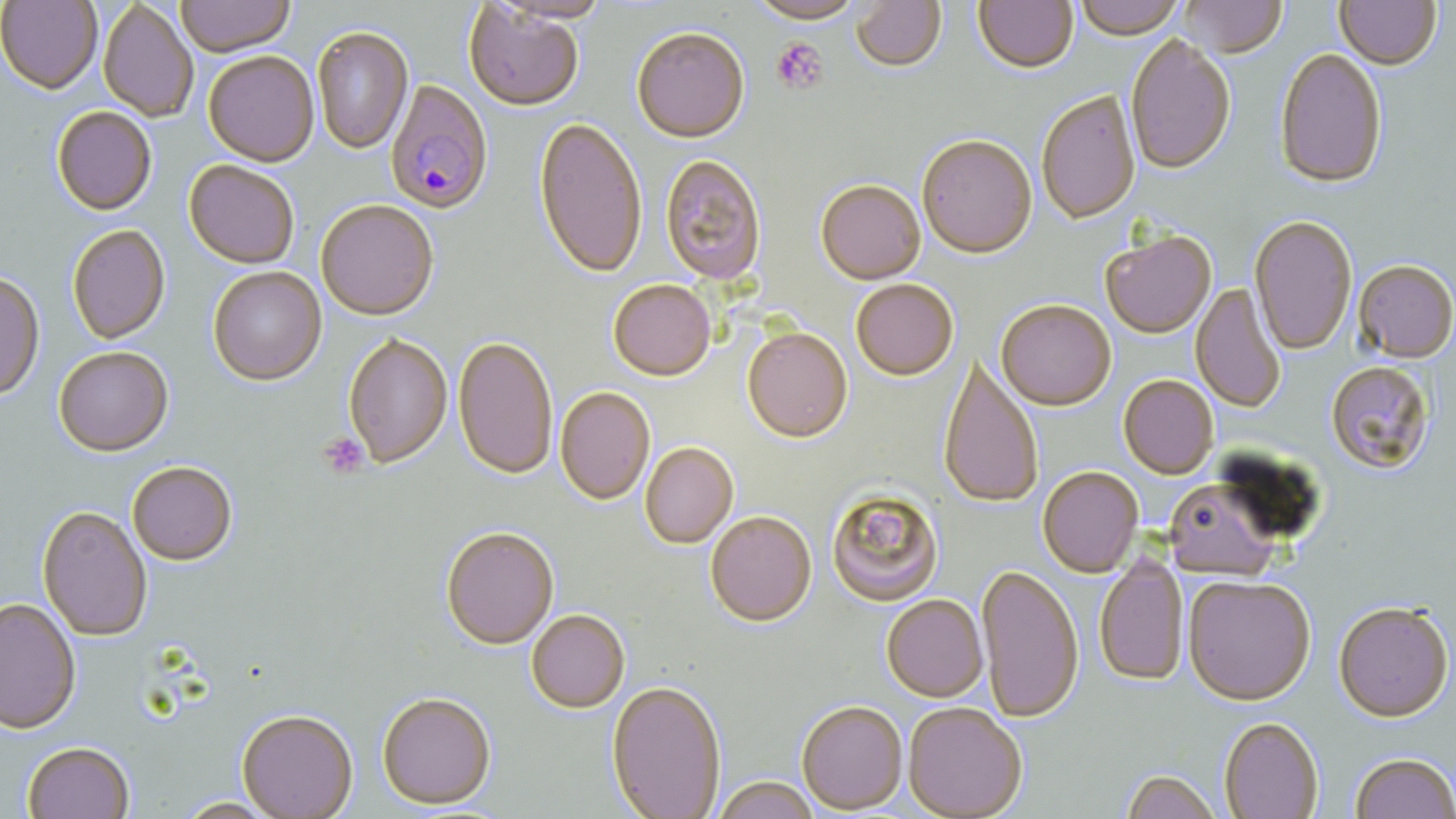
{
  "slide_level_diagnosis": "Plasmodium falciparum",
  "platelet_locations": "approximate bounding boxes as (x1, y1, x2, y2) in pixels: (772, 38, 829, 96), (319, 434, 372, 476)",
  "preparation": "thin blood smear",
  "image_size": "1456×819 pixels",
  "plasmodium_falciparum_infected_red_blood_cell_locations": "approximate bounding boxes as (x1, y1, x2, y2) in pixels: (386, 78, 494, 214)",
  "modality": "optical microscopy",
  "uninfected_red_blood_cell_locations": "approximate bounding boxes as (x1, y1, x2, y2) in pixels: (1, 0, 102, 92), (175, 0, 296, 55), (494, 0, 617, 23), (747, 0, 867, 25), (1074, 0, 1185, 39), (1180, 0, 1287, 58), (852, 1, 947, 72), (974, 1, 1079, 72), (1335, 1, 1443, 70), (97, 2, 200, 123), (462, 2, 585, 111), (311, 24, 413, 154), (632, 24, 752, 142), (1122, 34, 1235, 176), (1274, 47, 1388, 188), (203, 50, 320, 165), (1034, 87, 1141, 225), (51, 105, 158, 215), (532, 115, 649, 279), (916, 132, 1037, 257), (659, 153, 768, 284), (185, 159, 301, 268), (815, 177, 927, 284), (315, 199, 438, 319), (1248, 215, 1360, 357), (65, 224, 170, 344), (1099, 228, 1218, 338), (1353, 258, 1455, 362), (205, 265, 326, 385), (0, 271, 44, 402), (850, 278, 958, 380), (607, 279, 718, 380), (1190, 283, 1287, 414), (995, 297, 1117, 410), (743, 326, 852, 441), (342, 331, 453, 468), (454, 335, 559, 479), (54, 347, 172, 456), (938, 359, 1043, 509), (1324, 360, 1436, 476), (1117, 373, 1219, 478), (554, 386, 656, 506), (640, 441, 738, 549), (127, 460, 238, 565), (1037, 464, 1142, 578), (1162, 477, 1283, 578), (827, 485, 942, 604), (38, 505, 154, 640), (704, 509, 816, 627), (442, 524, 559, 649), (1094, 554, 1190, 685), (977, 562, 1085, 722), (1183, 572, 1315, 704), (880, 592, 988, 702), (0, 596, 80, 732), (1333, 599, 1454, 720), (525, 608, 629, 712), (606, 679, 727, 817), (376, 690, 497, 809), (795, 698, 906, 812), (903, 701, 1028, 819), (237, 707, 358, 818), (1218, 716, 1323, 819), (23, 741, 135, 819), (1348, 751, 1455, 819), (1120, 769, 1224, 818), (710, 775, 824, 818), (176, 797, 278, 817)",
  "field_of_view": "one of a larger specimen",
  "stain": "May-Grünwald-Giemsa",
  "magnification": "1000x"
}